Assess the morphology of the red blood cells.
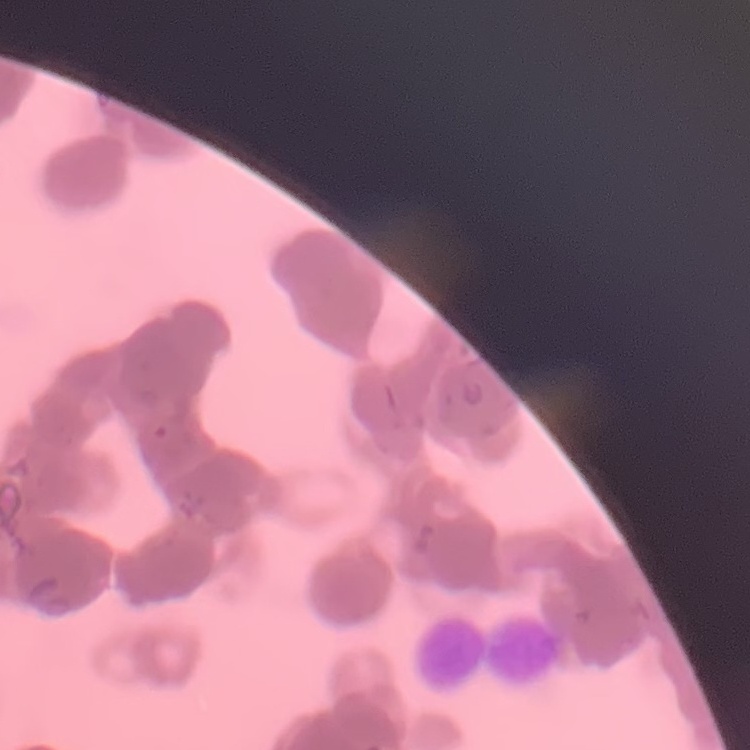

Rouleaux formation.

stain = Field's or Giemsa
preparation = thin peripheral smear
image type = square crop of a larger photomicrograph